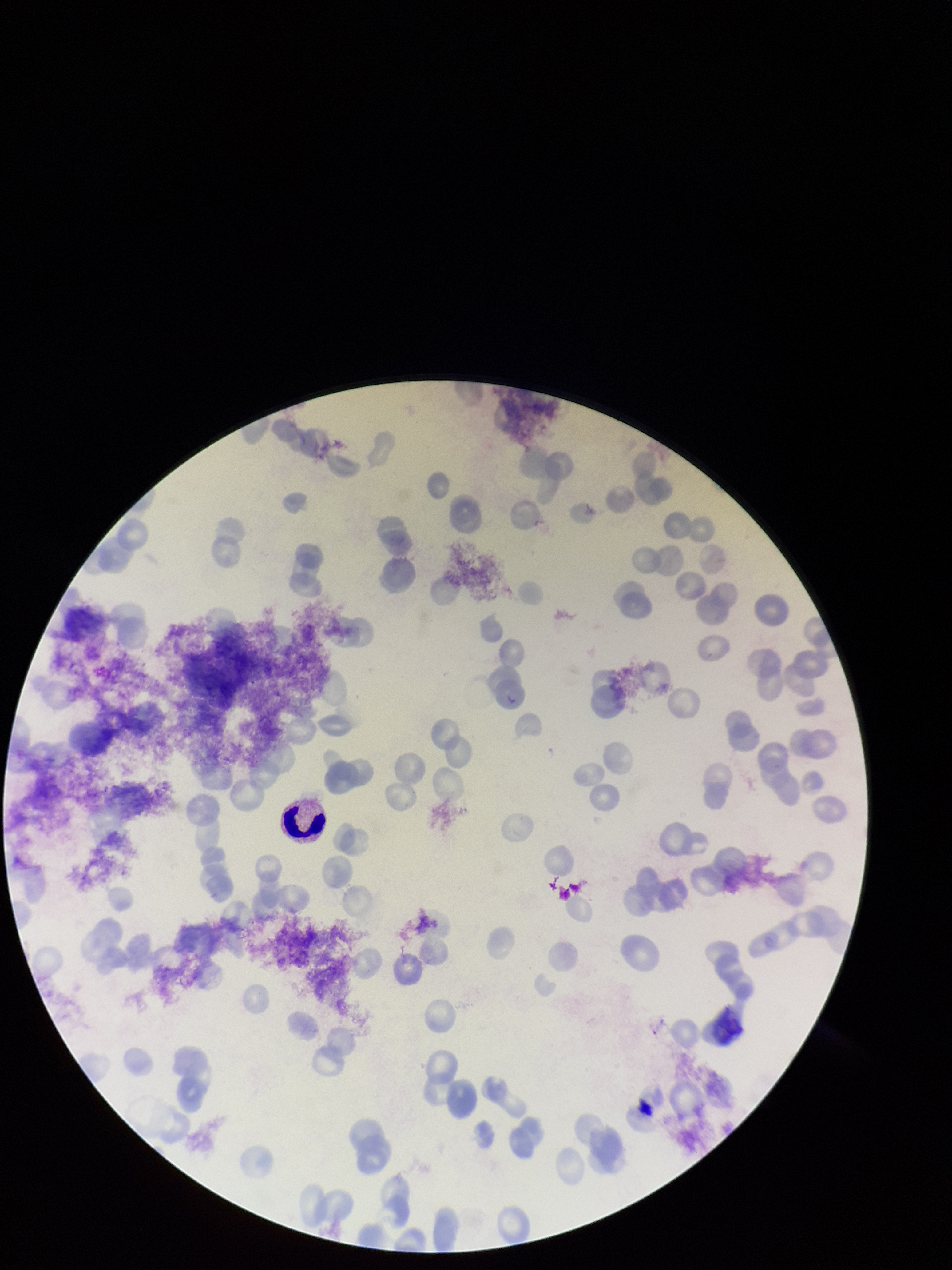
Summary:
  - Preparation: thin smear
  - Parasitized red blood cell count: 0
  - Image size: 952×1270 pixels
  - Stain: Giemsa
  - Capture: smartphone photograph through the microscope eyepiece
  - Red blood cell count: 102
  - Field of view: one from this slide
  - Patient malaria status: positive
  - Species reported for this patient: Plasmodium vivax
  - Parasitized red blood cells: none seen